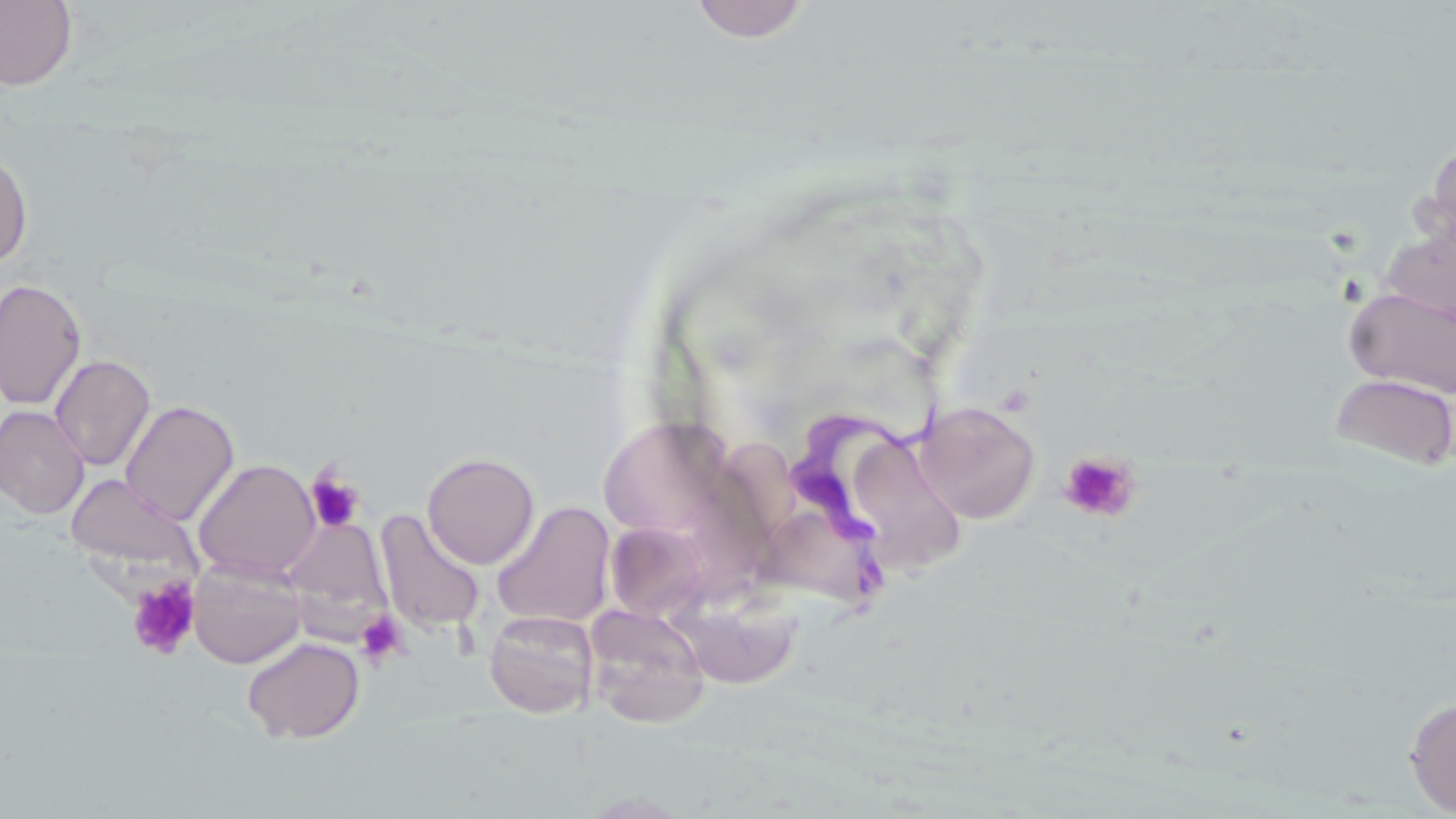

Summary:
  - Coordinate format: approximate bounding boxes as named x1/y1/x2/y2 corners in pixels
  - Platelet locations: (x1=1058, y1=450, x2=1142, y2=524), (x1=305, y1=468, x2=366, y2=533), (x1=127, y1=576, x2=201, y2=661), (x1=355, y1=609, x2=409, y2=667)
  - Trypanosoma brucei locations: (x1=788, y1=385, x2=948, y2=612)
  - Uninfected red blood cell locations: (x1=688, y1=0, x2=813, y2=43), (x1=0, y1=1, x2=78, y2=90), (x1=1416, y1=138, x2=1456, y2=266), (x1=0, y1=148, x2=34, y2=268), (x1=1380, y1=228, x2=1456, y2=331), (x1=0, y1=277, x2=87, y2=411), (x1=1344, y1=287, x2=1456, y2=398), (x1=49, y1=354, x2=156, y2=472), (x1=1330, y1=373, x2=1456, y2=471), (x1=120, y1=400, x2=240, y2=525), (x1=914, y1=401, x2=1041, y2=523), (x1=0, y1=405, x2=89, y2=519), (x1=598, y1=414, x2=736, y2=541), (x1=855, y1=435, x2=961, y2=556), (x1=700, y1=440, x2=804, y2=588), (x1=422, y1=451, x2=540, y2=569), (x1=193, y1=459, x2=320, y2=581), (x1=64, y1=473, x2=201, y2=575), (x1=491, y1=501, x2=616, y2=629), (x1=375, y1=510, x2=486, y2=635), (x1=757, y1=514, x2=875, y2=612), (x1=280, y1=517, x2=392, y2=630), (x1=605, y1=521, x2=711, y2=622), (x1=188, y1=558, x2=307, y2=669), (x1=671, y1=589, x2=804, y2=692), (x1=584, y1=604, x2=710, y2=729), (x1=484, y1=609, x2=599, y2=718), (x1=241, y1=636, x2=365, y2=745), (x1=1404, y1=695, x2=1456, y2=815)
  - Slide-level diagnosis: Trypanosoma brucei
  - Stain: May-Grünwald-Giemsa
  - Modality: light microscopy
  - Field of view: single
  - Preparation: thin blood film
  - Image size: 1456×819 pixels
  - Magnification: 1000x